Describe the morphology of the red blood cells.
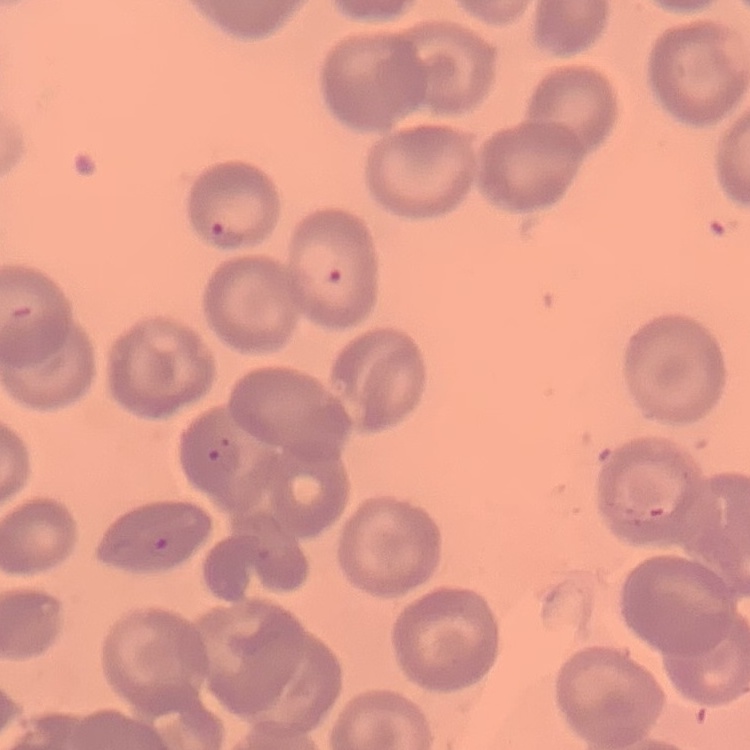

No rouleaux formation.

stain = Field's or Giemsa
image type = one tile cut from a larger photomicrograph
preparation = thin blood smear